Outline each blood parasite and name the species.
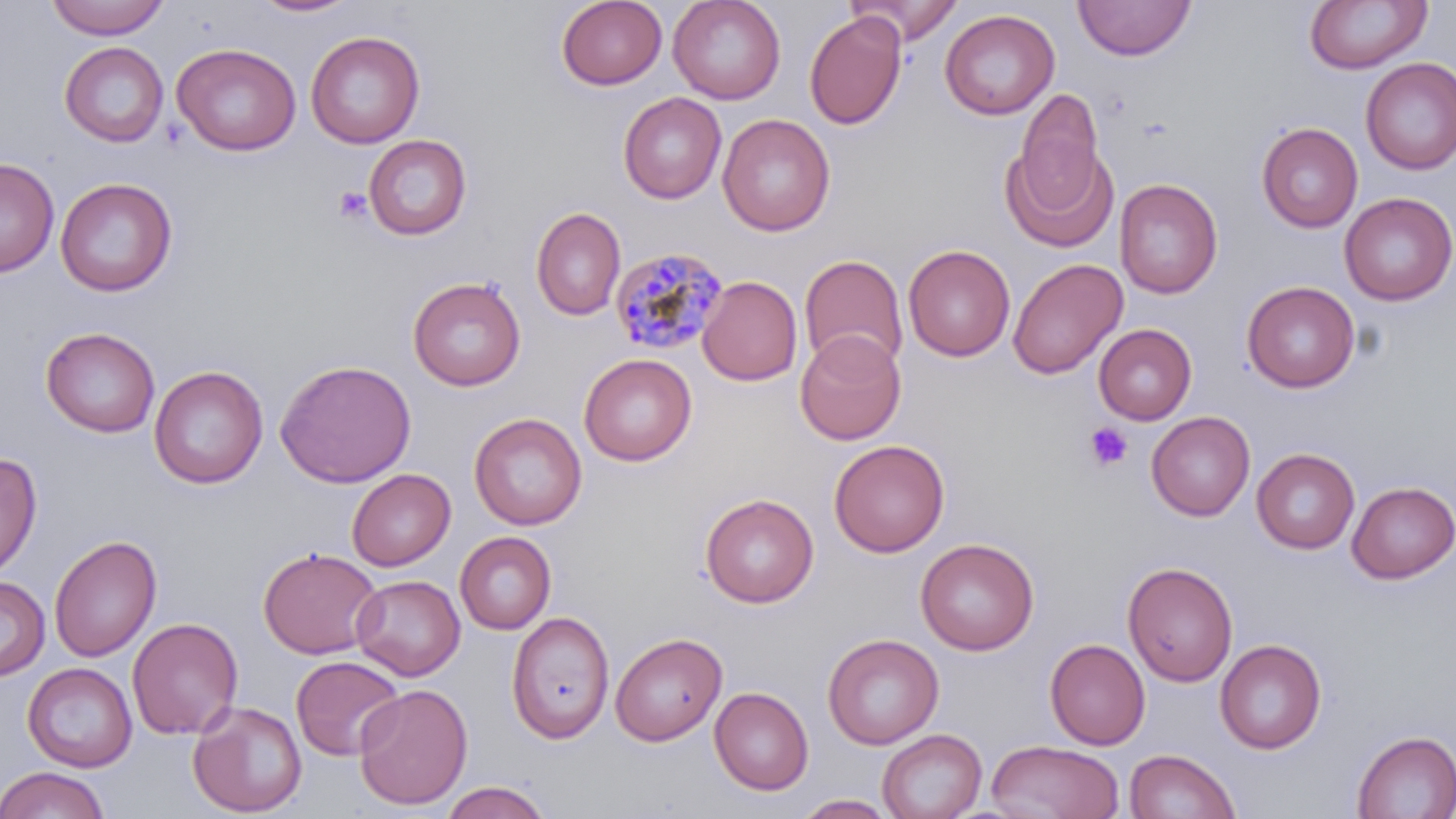
Approximate bounding boxes as (x1,y1)-(x2,y2) corner pairs in pixels.
Plasmodium malariae-infected red blood cells: (609,246)-(728,355).
No Plasmodium falciparum, Plasmodium ovale, Plasmodium vivax, Babesia divergens, or Trypanosoma brucei observed.

{
  "slide_level_diagnosis": "Plasmodium malariae",
  "preparation": "thin blood film",
  "platelet_locations": "approximate bounding boxes as (x1,y1)-(x2,y2) corner pairs in pixels: (332,187)-(372,222), (1084,421)-(1133,472)",
  "field_of_view": "single",
  "image_size": "1456×819 pixels",
  "uninfected_red_blood_cell_locations": "approximate bounding boxes as (x1,y1)-(x2,y2) corner pairs in pixels: (44,0)-(171,39), (668,0)-(785,104), (846,0)-(965,45), (1073,0)-(1195,60), (250,1)-(360,18), (556,1)-(667,90), (1304,1)-(1431,74), (939,8)-(1059,120), (804,11)-(906,130), (305,30)-(425,148), (59,41)-(169,147), (171,42)-(301,156), (1360,58)-(1456,175), (1016,88)-(1104,209), (618,92)-(726,204), (717,113)-(835,236), (1256,122)-(1363,232), (364,135)-(472,240), (1000,141)-(1117,253), (0,157)-(59,277), (55,177)-(178,297), (1115,178)-(1223,299), (1339,192)-(1455,305), (531,207)-(626,321), (903,244)-(1015,361), (800,254)-(908,372), (1008,259)-(1126,379), (698,275)-(802,386), (408,276)-(526,391), (1242,281)-(1360,392), (1093,323)-(1197,424), (40,326)-(161,437), (795,330)-(906,445), (579,353)-(697,466), (275,358)-(416,488), (149,365)-(268,489), (1146,411)-(1255,521), (469,412)-(587,530), (829,439)-(949,557), (1252,448)-(1360,553), (0,450)-(42,580), (347,468)-(456,570), (1346,480)-(1456,583), (700,493)-(818,607), (455,531)-(557,634), (49,534)-(161,663), (915,537)-(1039,655), (258,546)-(382,659), (1122,560)-(1238,687), (352,575)-(465,680), (0,576)-(50,681), (506,611)-(615,743), (127,617)-(244,740), (611,632)-(727,745), (823,633)-(944,749), (1045,638)-(1150,749), (1215,638)-(1327,753), (291,655)-(406,761), (22,662)-(137,772), (354,683)-(473,810), (709,686)-(813,795), (187,699)-(308,817), (878,728)-(986,819), (1352,730)-(1455,819), (986,740)-(1125,819), (1124,748)-(1240,819), (0,766)-(111,818), (437,781)-(555,819), (794,795)-(898,818)",
  "stain": "May-Grünwald-Giemsa",
  "magnification": "1000x",
  "modality": "light microscopy"
}